Report the malaria status of this cell.
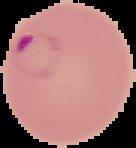

It is parasitized.

Image is 136×148 pixels. The area outside the segmented cell region is set to black. From a thin blood film.